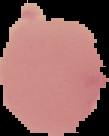

image type = cell region segmented out of the field of view; surrounding area masked to black
preparation = thin blood smear
image size = 109×136 pixels
malaria status = uninfected